Locate leukocytes (white blood cells).
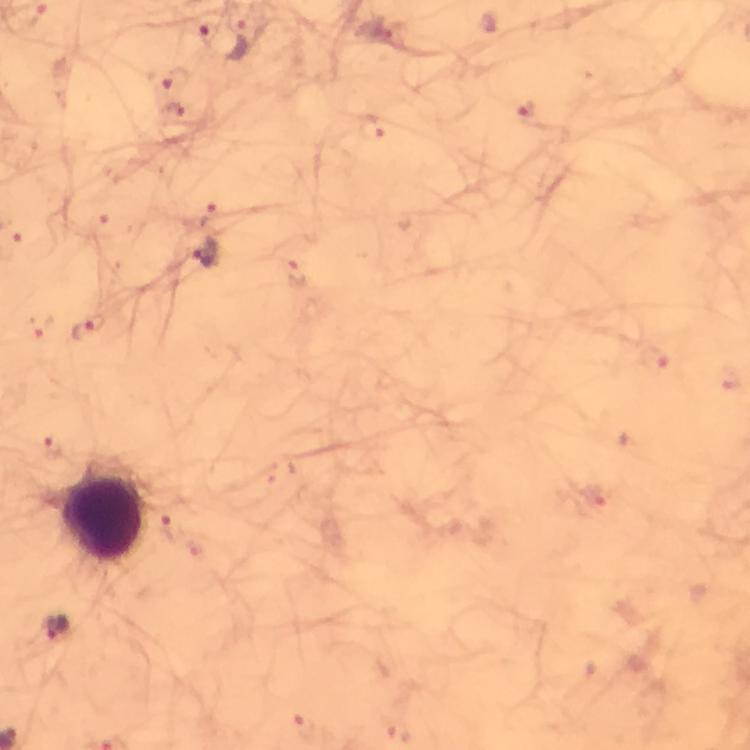

Approximate object centers, in pixels from the top-left corner.
Leukocytes: (x=103, y=519).

cropped_from: one field of view
immersion_oil: applied
context: from a malaria diagnostic workup
stain: Giemsa
capture: smartphone photograph through a microscope
image_size: 750×750 pixels
plasmodium_parasite_locations: 'approximate object centers, in pixels from the top-left corner: (x=204, y=30), (x=238, y=43), (x=173, y=78), (x=171, y=112), (x=530, y=113), (x=371, y=127), (x=209, y=214), (x=205, y=253), (x=297, y=273), (x=89, y=330), (x=655, y=359), (x=53, y=447), (x=172, y=525), (x=55, y=628), (x=397, y=731)'
magnification: 100x
preparation: thick smear